Report the malaria status of this cell.
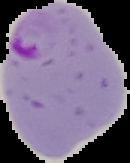

Parasitized.

image size = 130×163 pixels
preparation = thin blood smear
image type = segmented cell region with the area outside set to black